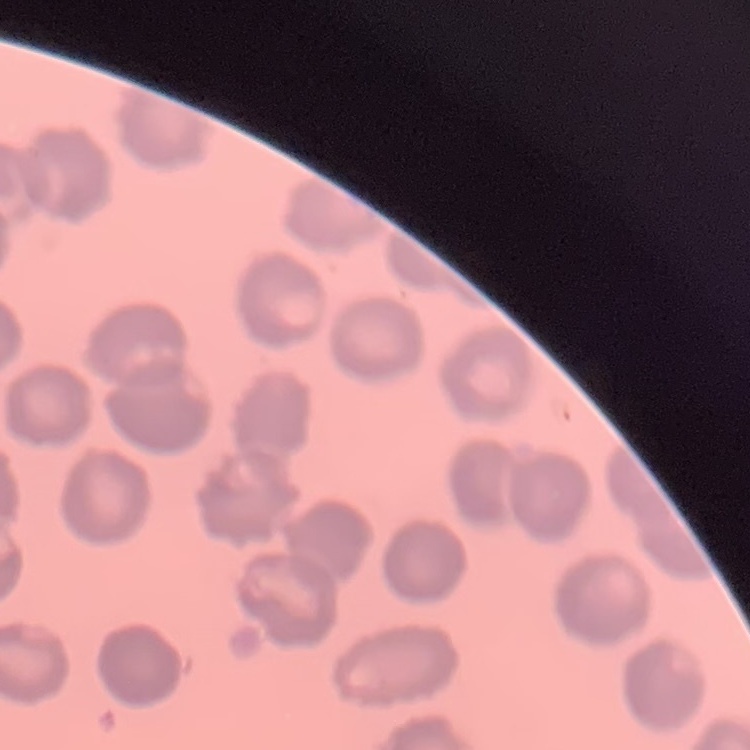
{
  "erythrocyte_morphology": "no rouleaux formation",
  "stain": "Field's or Giemsa",
  "image_type": "one tile cut from a larger photomicrograph",
  "preparation": "thin blood smear"
}